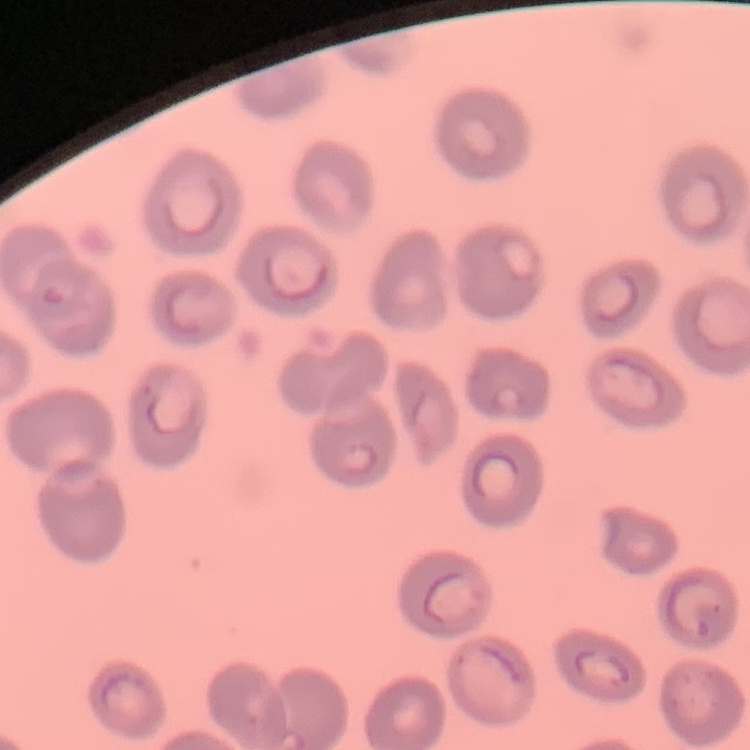
red blood cell morphology = no rouleaux formation
stain = Field's or Giemsa
image type = one tile cut from a larger photomicrograph
preparation = thin blood smear